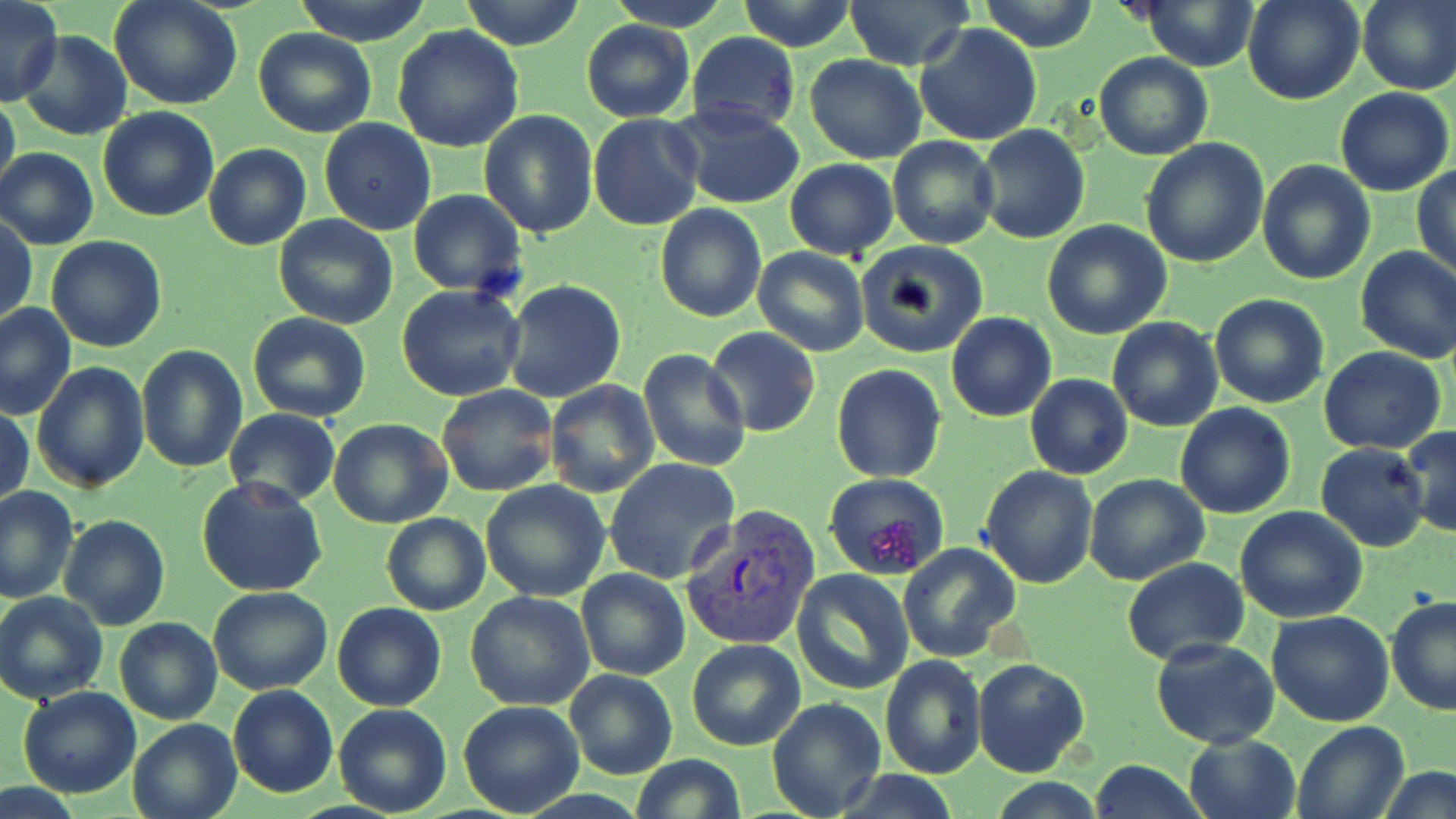
Approximate bounding boxes as [x1, y1, x2, y2] in pixels. Plasmodium vivax-infected red blood cell locations: [681, 507, 822, 652]. Uninfected red blood cell locations: [110, 0, 242, 110], [292, 0, 435, 45], [461, 0, 585, 50], [605, 0, 733, 31], [738, 0, 854, 51], [843, 0, 977, 70], [978, 0, 1101, 53], [1241, 0, 1364, 106], [1357, 0, 1456, 94], [0, 2, 62, 106], [1137, 2, 1262, 71], [581, 20, 694, 122], [913, 23, 1043, 148], [393, 24, 524, 153], [253, 28, 376, 137], [18, 30, 132, 141], [687, 31, 800, 133], [1094, 52, 1214, 161], [806, 54, 926, 164], [1336, 88, 1454, 195], [0, 92, 21, 203], [671, 103, 806, 208], [97, 105, 219, 222], [479, 110, 599, 239], [589, 113, 705, 230], [318, 119, 436, 236], [974, 125, 1090, 244], [887, 135, 999, 249], [1140, 139, 1270, 269], [204, 144, 311, 251], [1, 146, 99, 251], [784, 158, 898, 260], [1257, 158, 1375, 284], [1412, 164, 1456, 278], [408, 190, 526, 295], [654, 204, 766, 322], [273, 215, 399, 330], [1041, 219, 1172, 339], [1, 220, 36, 326], [44, 237, 166, 353], [854, 240, 990, 358], [1354, 246, 1456, 364], [752, 247, 870, 357], [501, 279, 628, 404], [396, 285, 526, 402], [1209, 293, 1329, 408], [1, 303, 76, 421], [248, 311, 372, 422], [945, 312, 1056, 422], [1104, 316, 1223, 431], [703, 328, 820, 437], [136, 345, 248, 473], [1318, 347, 1446, 455], [636, 348, 752, 471], [32, 361, 149, 493], [830, 364, 946, 483], [1025, 373, 1132, 481], [546, 381, 660, 499], [435, 384, 558, 498], [1173, 403, 1295, 519], [1, 405, 34, 508], [225, 408, 339, 506], [329, 418, 453, 529], [1400, 424, 1456, 538], [1315, 442, 1430, 552], [604, 457, 741, 583], [978, 466, 1099, 587], [824, 472, 949, 580], [1084, 474, 1210, 586], [196, 478, 328, 600], [480, 480, 610, 602], [0, 486, 77, 602], [1234, 507, 1368, 623], [381, 512, 490, 615], [59, 514, 169, 630], [896, 543, 1021, 663], [1122, 558, 1250, 665], [575, 568, 689, 680], [792, 568, 914, 694], [208, 586, 333, 695], [466, 591, 596, 711], [1, 592, 108, 705], [1386, 596, 1456, 716], [333, 601, 446, 711], [1267, 610, 1396, 727], [114, 616, 223, 725], [1151, 637, 1279, 748], [687, 638, 806, 751], [879, 653, 986, 778], [972, 656, 1089, 777], [565, 667, 677, 780], [228, 685, 339, 798], [19, 686, 140, 798], [767, 697, 887, 819], [458, 701, 585, 817], [334, 704, 452, 816], [127, 717, 242, 819], [1292, 719, 1410, 819], [1183, 733, 1302, 819], [629, 753, 747, 819], [1091, 759, 1208, 818], [1378, 765, 1456, 819]. Slide-level diagnosis: Plasmodium vivax. May-Grünwald-Giemsa-stained preparation. One field of a larger specimen. Image is 1456×819 pixels. Captured at 1000x magnification. Optical microscopy. Thin blood smear.